Classify this cell by malaria status.
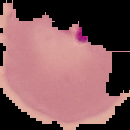
It is parasitized.

From a thin blood smear. Image is 130×130 pixels. Cell region segmented out of the field of view; the surrounding area is masked to black.